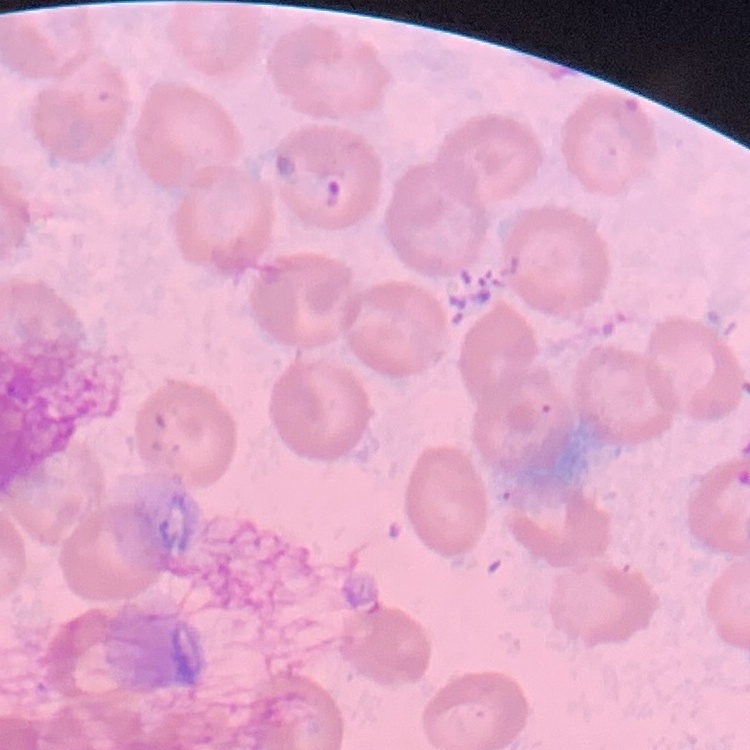 The erythrocytes show no rouleaux formation. Thin peripheral smear. One tile cut from a larger photomicrograph. Field's or Giemsa stain.